State which parasite is depicted.
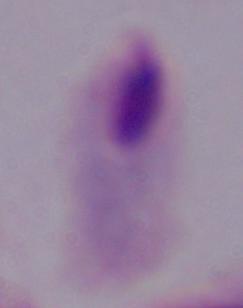

A trichomonad.

modality = photomicrograph
magnification = 1000x